Identify the preparation type.
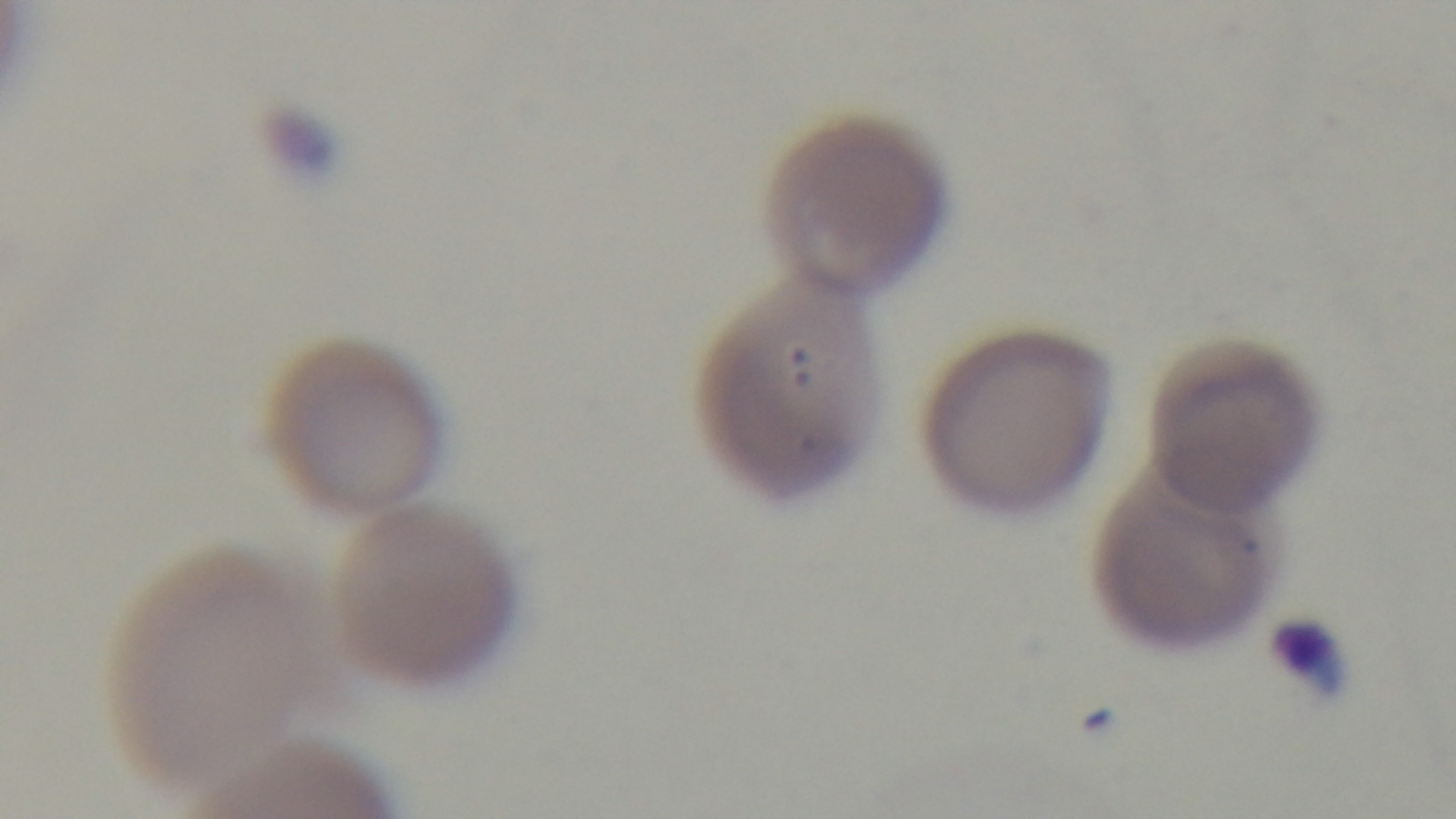

It is a thin blood film.

objective: 100x oil immersion
stain: Giemsa
field_of_view: one from the slide
modality: light microscopy
malaria_status: positive
capture: mounted 4K digital camera